Assess the morphology of the erythrocytes.
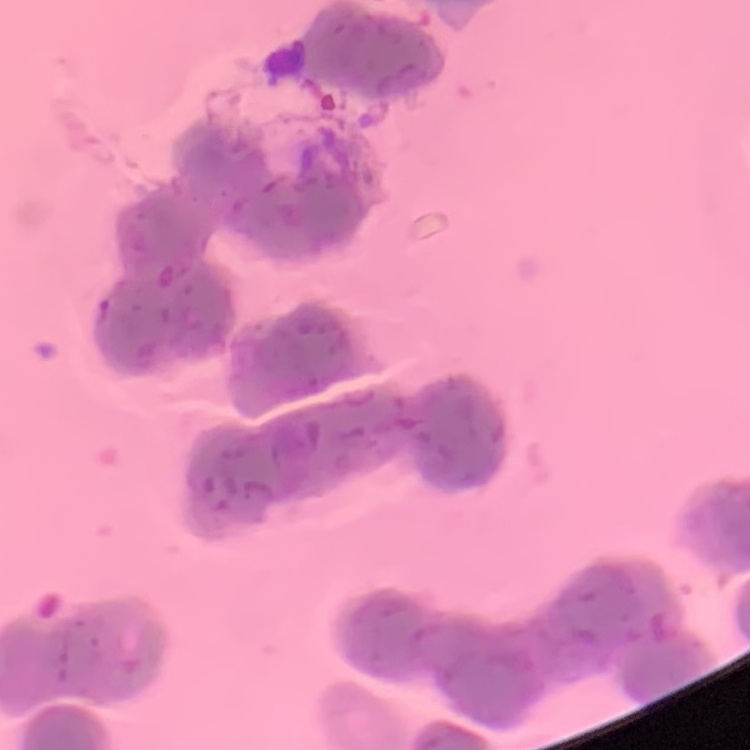
They show rouleaux formation.

preparation = thin blood smear
image type = square crop of a larger photomicrograph
stain = Field's or Giemsa